Assess this cell for malaria.
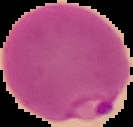
It is parasitized.

Summary:
  - Preparation: thin blood smear
  - Image size: 133×127 pixels
  - Image type: cell region segmented out of the field of view; surrounding area masked to black